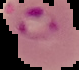

malaria status = parasitized
image size = 79×70 pixels
preparation = thin blood smear
image type = segmented cell region with the area outside set to black